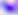

identification = Toxoplasma gondii
modality = photomicrograph
magnification = 400x